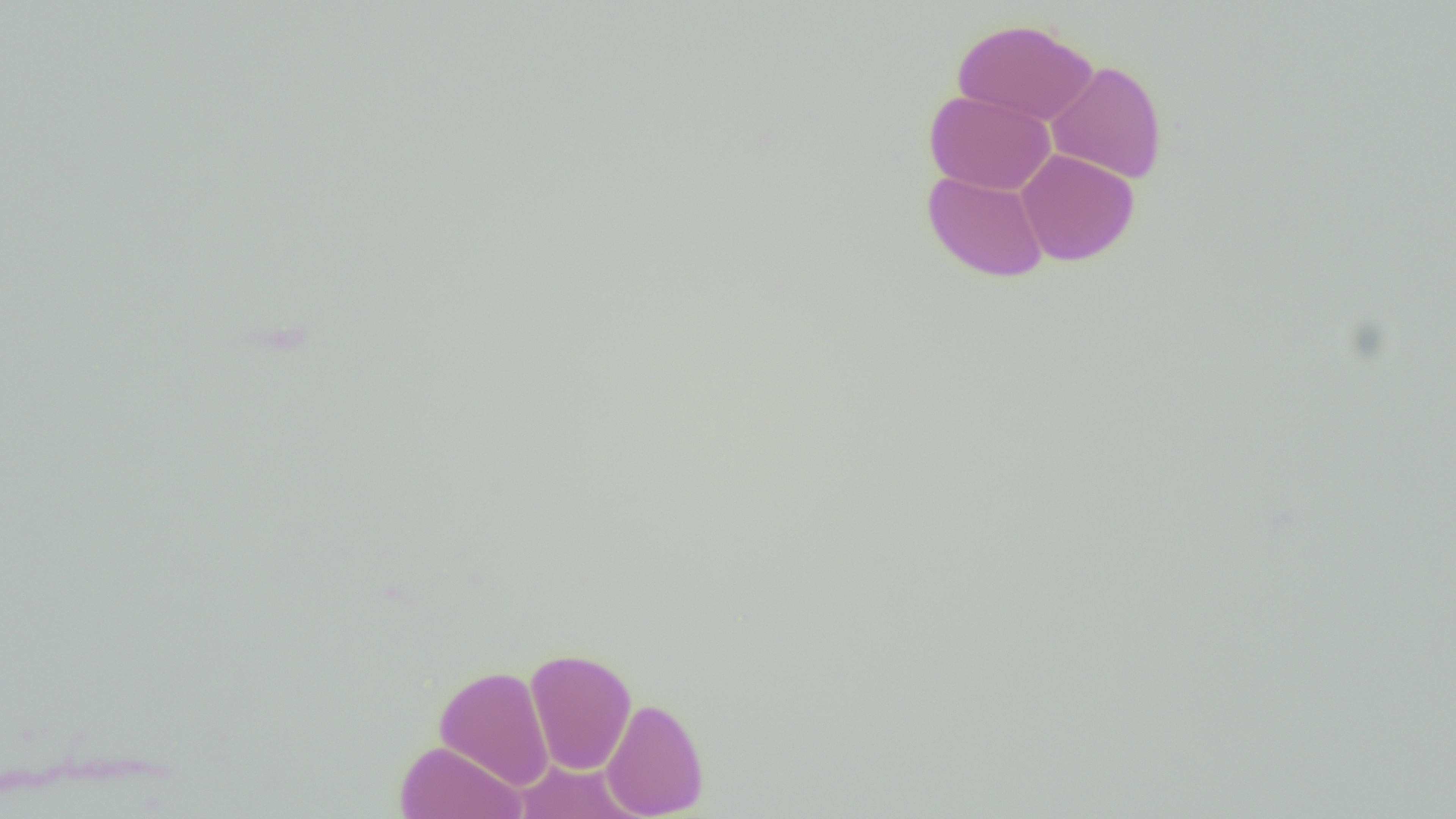
slide-level diagnosis = no evidence of blood parasites
uninfected red blood cell locations = approximate bounding boxes as (x1,y1)-(x2,y2) corner pairs in pixels: (952,18)-(1098,125), (1046,59)-(1167,184), (924,90)-(1055,195), (1016,148)-(1139,266), (923,169)-(1048,282), (525,647)-(637,775), (434,665)-(555,791), (600,696)-(709,818), (394,740)-(526,819), (514,759)-(641,818)
modality = light microscopy
field of view = one of a larger specimen
preparation = thin blood film
image size = 1456×819 pixels
magnification = 1000x